Assess this cell for malaria.
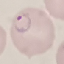

It is parasitized.

{
  "image_type": "automatically extracted cell patch, resized to 64 × 64 pixels",
  "stain": "Giemsa",
  "preparation": "thin blood smear",
  "capture": "smartphone camera at the microscope eyepiece"
}